Classify this cell by malaria status.
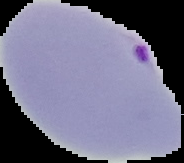
Parasitized.

Image is 184×163 pixels. From a thin blood smear. Segmented cell region on a black background.